Assess this cell for malaria.
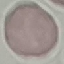

It is uninfected.

{
  "stain": "Giemsa",
  "capture": "smartphone camera at the microscope eyepiece",
  "preparation": "thin blood smear",
  "image_type": "automatically extracted cell patch, resized to 64 × 64 pixels"
}